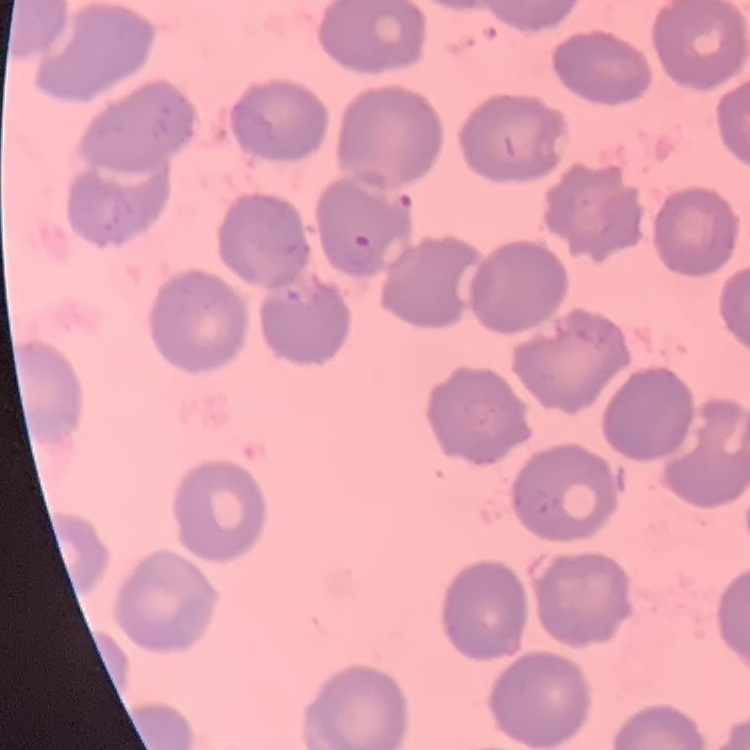

Summary:
  - Red blood cell morphology: no rouleaux formation
  - Stain: Field's or Giemsa
  - Image type: one tile cut from a larger photomicrograph
  - Preparation: thin blood smear